Locate every Plasmodium parasite.
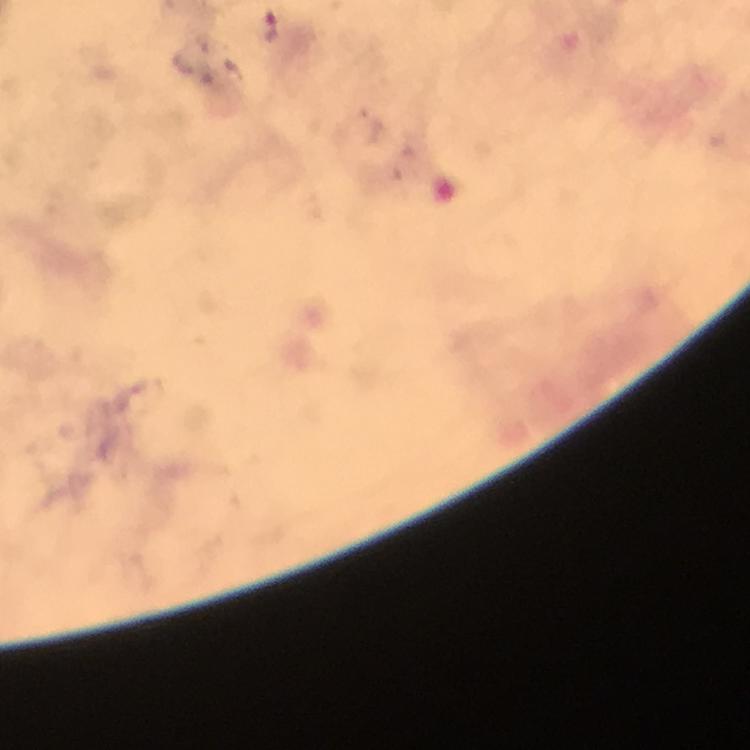

Approximate centers as [x, y] in pixels.
Plasmodium parasites: [271, 26].

context = from a diagnostic examination for malaria
cropped from = a single field of view
image size = 750×750 pixels
preparation = thick smear
immersion oil = applied
stain = Giemsa
capture = smartphone photograph through a microscope
magnification = 100x